Name the blood parasite species.
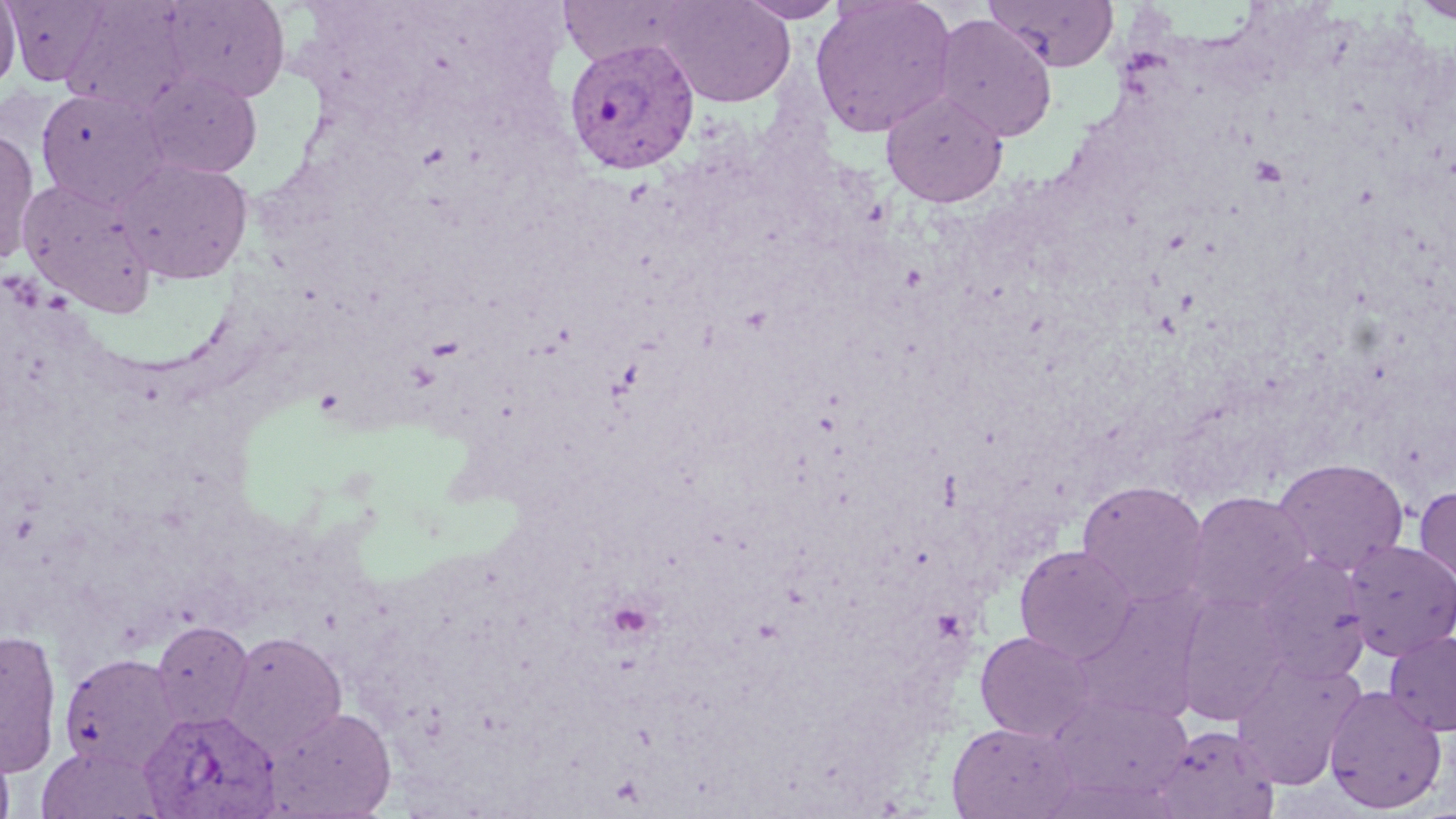

Plasmodium vivax.

Approximate bounding boxes as named x1/y1/x2/y2 corners in pixels. Plasmodium vivax-infected red blood cell locations: (x1=563, y1=37, x2=700, y2=175), (x1=139, y1=708, x2=281, y2=818). Platelet locations: (x1=1247, y1=154, x2=1288, y2=188), (x1=425, y1=335, x2=466, y2=361), (x1=315, y1=388, x2=345, y2=414), (x1=605, y1=601, x2=656, y2=641), (x1=931, y1=609, x2=967, y2=642). Uninfected red blood cell locations: (x1=0, y1=0, x2=21, y2=93), (x1=5, y1=0, x2=112, y2=85), (x1=159, y1=0, x2=290, y2=103), (x1=655, y1=0, x2=796, y2=108), (x1=735, y1=0, x2=846, y2=23), (x1=810, y1=0, x2=958, y2=138), (x1=982, y1=0, x2=1119, y2=72), (x1=1411, y1=1, x2=1456, y2=24), (x1=932, y1=13, x2=1058, y2=143), (x1=141, y1=72, x2=262, y2=179), (x1=35, y1=88, x2=168, y2=207), (x1=881, y1=89, x2=1008, y2=207), (x1=0, y1=129, x2=39, y2=263), (x1=117, y1=157, x2=253, y2=284), (x1=17, y1=178, x2=156, y2=316), (x1=1272, y1=458, x2=1409, y2=576), (x1=1076, y1=479, x2=1210, y2=609), (x1=1414, y1=484, x2=1456, y2=591), (x1=1185, y1=491, x2=1313, y2=614), (x1=1343, y1=539, x2=1456, y2=660), (x1=1014, y1=544, x2=1138, y2=665), (x1=1251, y1=554, x2=1371, y2=683), (x1=1069, y1=588, x2=1205, y2=724), (x1=1175, y1=591, x2=1289, y2=724), (x1=150, y1=620, x2=255, y2=730), (x1=0, y1=628, x2=62, y2=778), (x1=223, y1=631, x2=348, y2=757), (x1=975, y1=631, x2=1094, y2=741), (x1=1385, y1=631, x2=1456, y2=736), (x1=59, y1=653, x2=182, y2=772), (x1=1232, y1=657, x2=1366, y2=790), (x1=1324, y1=684, x2=1448, y2=814), (x1=1050, y1=694, x2=1193, y2=801), (x1=265, y1=706, x2=397, y2=817), (x1=945, y1=721, x2=1076, y2=818), (x1=1153, y1=724, x2=1280, y2=819), (x1=0, y1=741, x2=15, y2=819). May-Grünwald-Giemsa stain. Image is 1456×819 pixels. Optical microscopy. 1000x magnification. One field of a larger specimen. Thin blood smear.